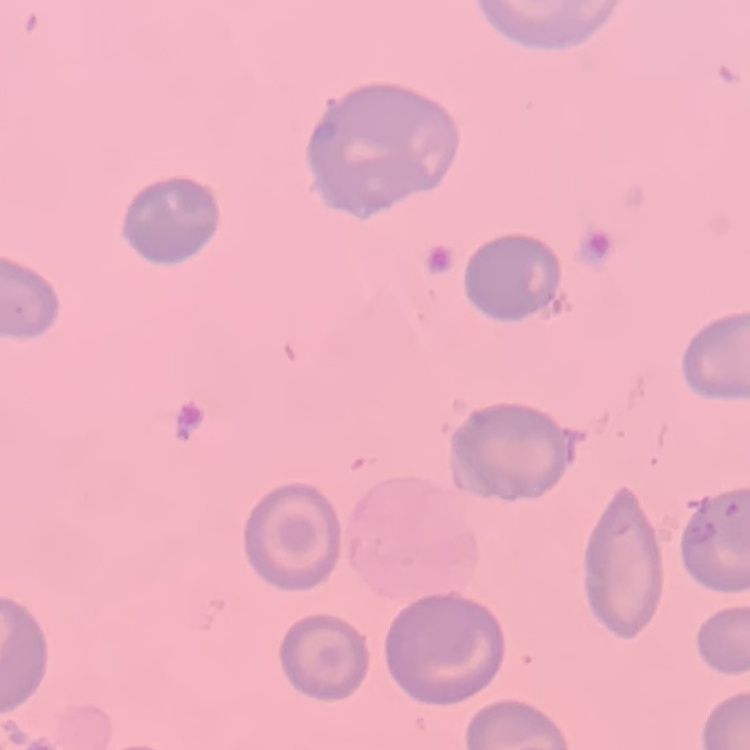
The erythrocytes show no rouleaux formation. Stained with either Field's or Giemsa. Square crop of a larger photomicrograph. Thin blood smear.